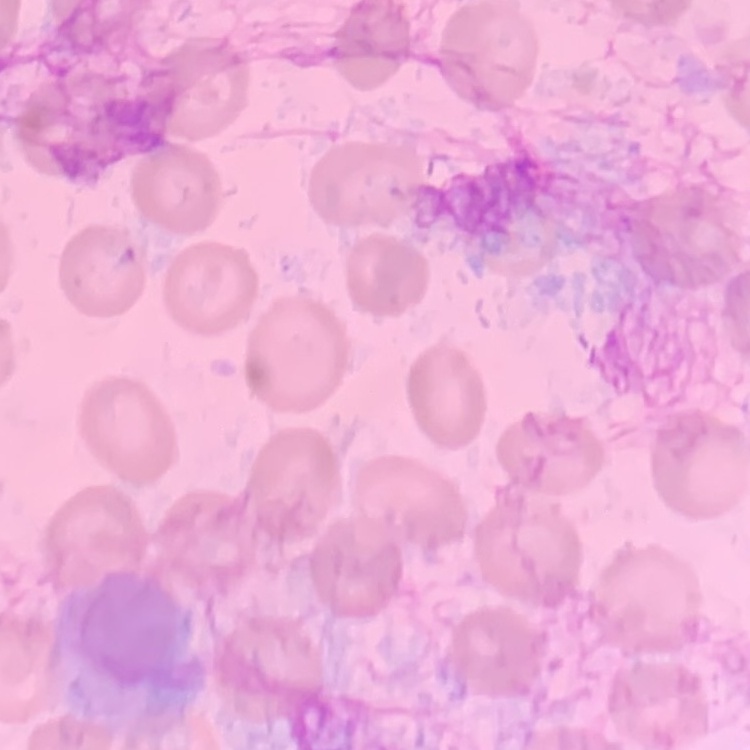 The red blood cells show no rouleaux formation. Thin blood film. Field's or Giemsa stain. One tile cut from a larger photomicrograph.